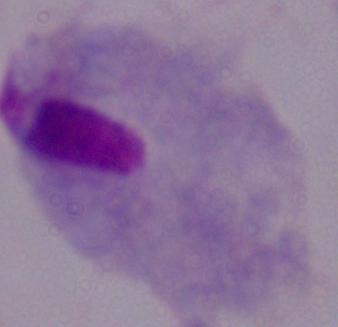
A trichomonad is seen. Micrograph. 1000x magnification.